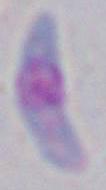 Captured at 1000x magnification. Photomicrograph. Toxoplasma gondii is seen.